Classify this cell by malaria status.
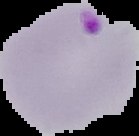

Parasitized.

{
  "image_type": "segmented cell region on a black background",
  "preparation": "thin blood film",
  "image_size": "139×136 pixels"
}